Give the preparation type.
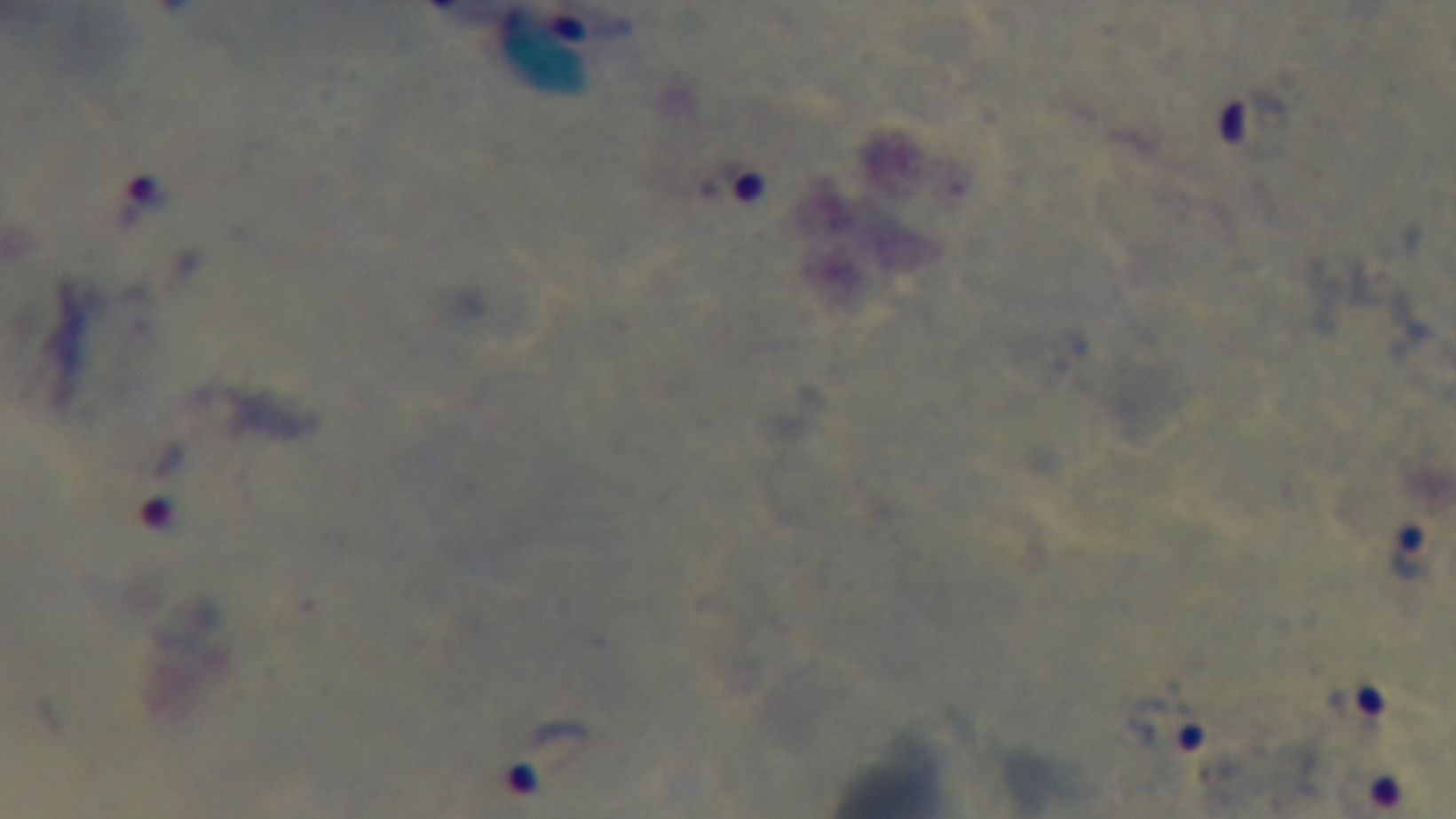
A thick smear.

stain: Giemsa
field_of_view: single
objective: 100x oil immersion
modality: light microscopy
malaria_status: infected
capture: mounted 4K digital camera